Report the malaria status.
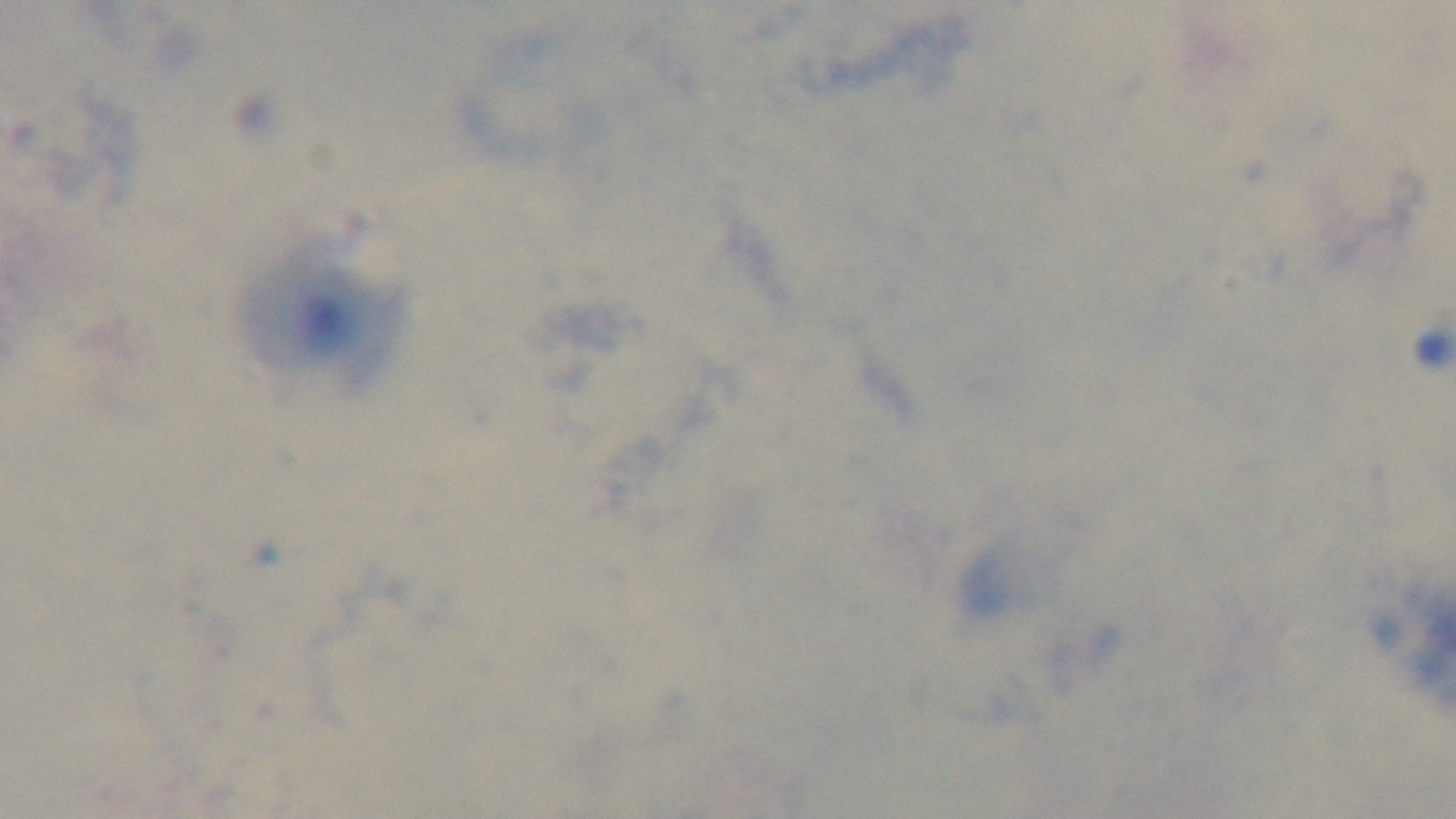
Uninfected.

{
  "capture": "mounted 4K digital camera",
  "modality": "light microscopy",
  "preparation": "thick smear",
  "stain": "Giemsa",
  "field_of_view": "one from the slide",
  "objective": "100x oil immersion"
}